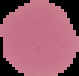

Summary:
  - Result: no malaria parasites seen
  - Image size: 79×76 pixels
  - Image type: segmented cell region on a black background
  - Preparation: thin blood smear